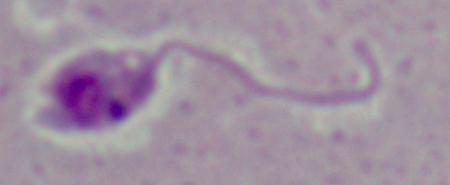

Summary:
  - Modality: photomicrograph
  - Magnification: 1000x
  - Identification: Leishmania